Describe the morphology of the erythrocytes.
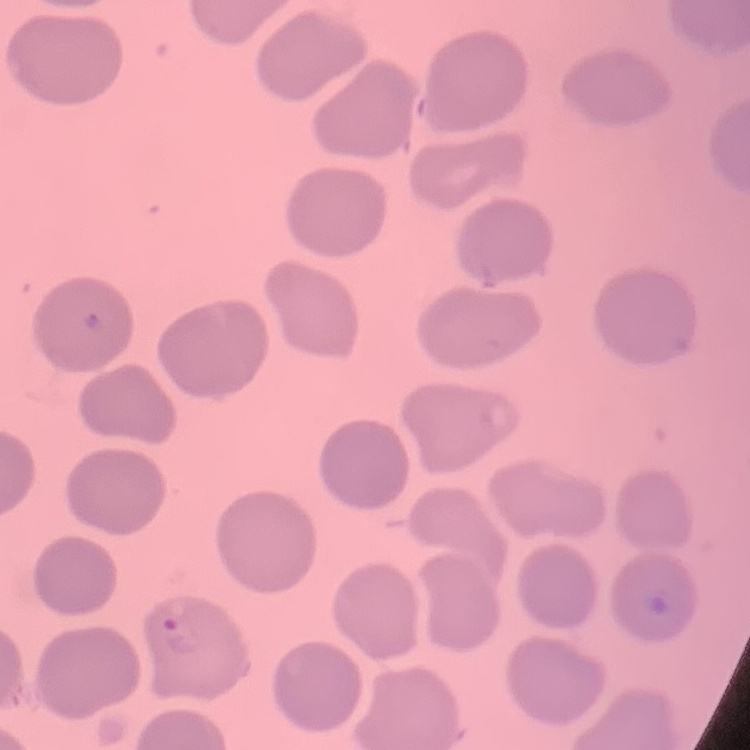

No rouleaux formation.

Thin peripheral smear. Square crop of a larger photomicrograph. Field's or Giemsa stain.